Locate every Plasmodium ovale-infected red blood cell.
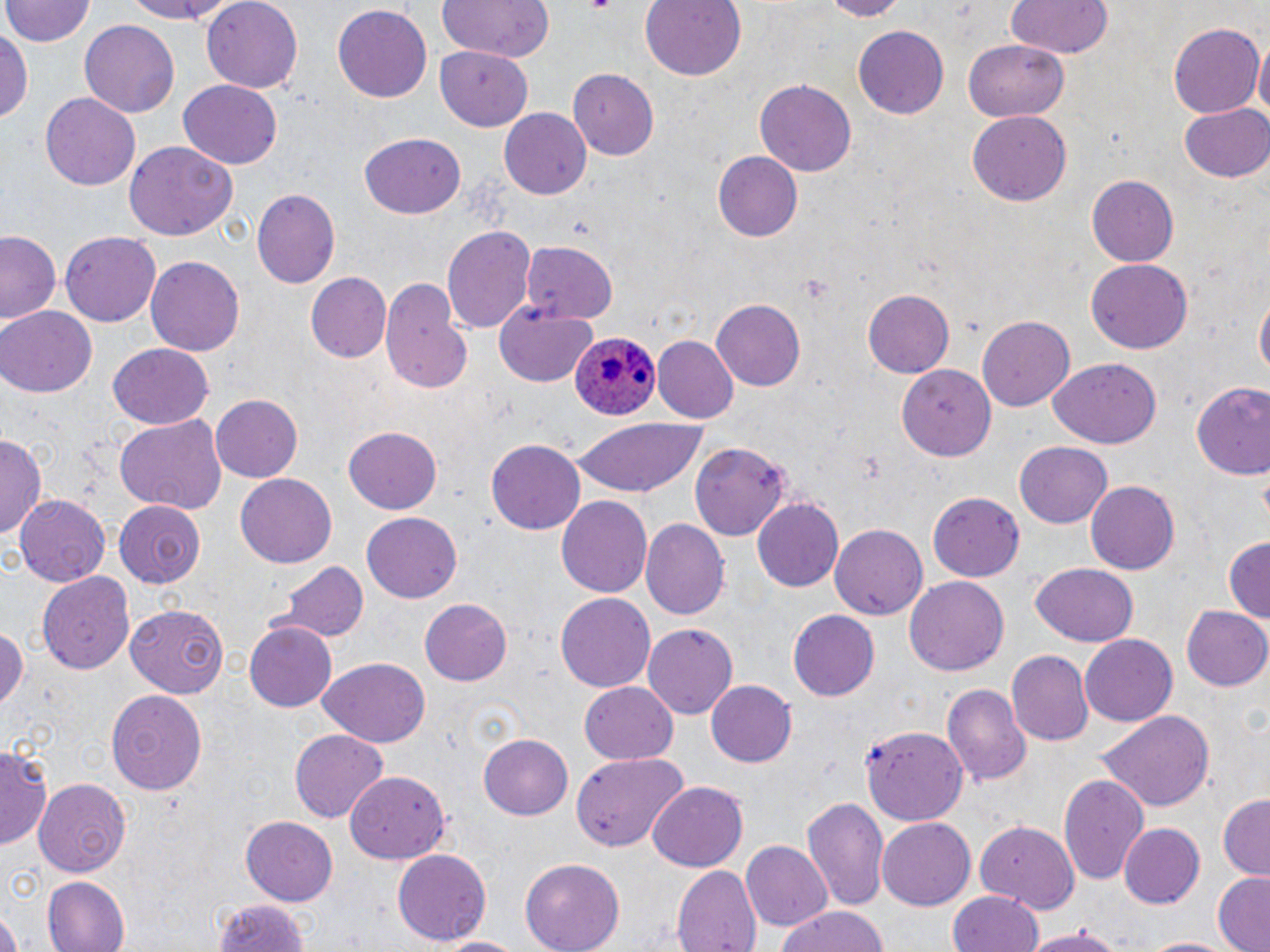
Approximate bounding boxes as (x1,y1)-(x2,y2) corner pairs in pixels.
Plasmodium ovale-infected red blood cells: (567,333)-(659,421).

Uninfected red blood cell locations: (3,0)-(94,47), (113,0)-(246,24), (201,0)-(306,90), (438,0)-(554,63), (640,0)-(746,80), (818,0)-(909,20), (1005,0)-(1113,60), (331,5)-(432,104), (80,20)-(179,117), (1168,23)-(1263,117), (1,24)-(31,129), (852,24)-(949,117), (1254,37)-(1269,131), (962,39)-(1071,120), (435,46)-(534,131), (567,67)-(661,161), (756,79)-(856,176), (178,80)-(280,169), (41,94)-(139,188), (1177,103)-(1270,185), (500,108)-(591,200), (967,111)-(1071,206), (357,133)-(466,218), (124,141)-(238,241), (712,151)-(802,241), (1088,175)-(1179,267), (251,188)-(339,288), (442,226)-(535,337), (0,229)-(62,328), (62,232)-(161,326), (517,241)-(617,323), (145,255)-(246,355), (1085,258)-(1193,354), (303,272)-(393,363), (380,276)-(468,395), (863,289)-(954,377), (1254,291)-(1268,384), (710,300)-(806,390), (493,303)-(600,385), (0,306)-(97,397), (977,317)-(1073,411), (652,336)-(737,423), (108,343)-(215,430), (1046,358)-(1161,448), (899,365)-(994,459), (1188,382)-(1270,482), (210,394)-(304,483), (569,416)-(711,497), (114,417)-(225,514), (344,427)-(443,514), (1,433)-(45,544), (487,440)-(585,533), (1014,441)-(1114,528), (690,445)-(789,539), (235,475)-(337,566), (1086,480)-(1180,574), (929,493)-(1025,581), (556,494)-(656,597), (12,496)-(112,586), (752,498)-(843,591), (114,500)-(206,588), (361,513)-(462,602), (641,518)-(729,618), (831,523)-(929,619), (1224,536)-(1269,627), (277,559)-(368,644), (1029,563)-(1139,648), (38,571)-(134,675), (905,576)-(1009,676), (555,591)-(656,693), (421,600)-(512,684), (125,602)-(231,695), (1181,605)-(1270,692), (788,609)-(880,701), (245,621)-(337,712), (0,623)-(26,713), (644,623)-(737,718), (1080,635)-(1177,725), (1008,651)-(1094,744), (318,658)-(430,746), (706,679)-(797,767), (580,680)-(677,764), (942,682)-(1031,789), (104,689)-(210,796), (1097,708)-(1216,813), (861,724)-(966,824), (290,730)-(386,820), (479,734)-(572,819), (1,743)-(54,849), (569,750)-(687,853), (1058,771)-(1150,886), (345,772)-(452,864), (35,779)-(132,876), (647,781)-(749,871), (802,794)-(888,911), (1216,795)-(1270,879), (239,816)-(339,905), (878,819)-(976,911), (975,819)-(1078,911), (1121,823)-(1204,908), (740,839)-(832,929), (391,849)-(492,945), (519,858)-(625,952), (671,865)-(762,952), (1212,873)-(1269,952), (42,876)-(131,952), (949,891)-(1043,952), (213,897)-(315,952), (776,904)-(889,952), (0,912)-(22,952), (1020,926)-(1128,951), (426,933)-(526,951), (1135,936)-(1240,952). Slide-level diagnosis: Plasmodium ovale. Image is 1270×952 pixels. Thin blood film. Captured at 1000x magnification. May-Grünwald-Giemsa stain. Single field of view. Light microscopy.